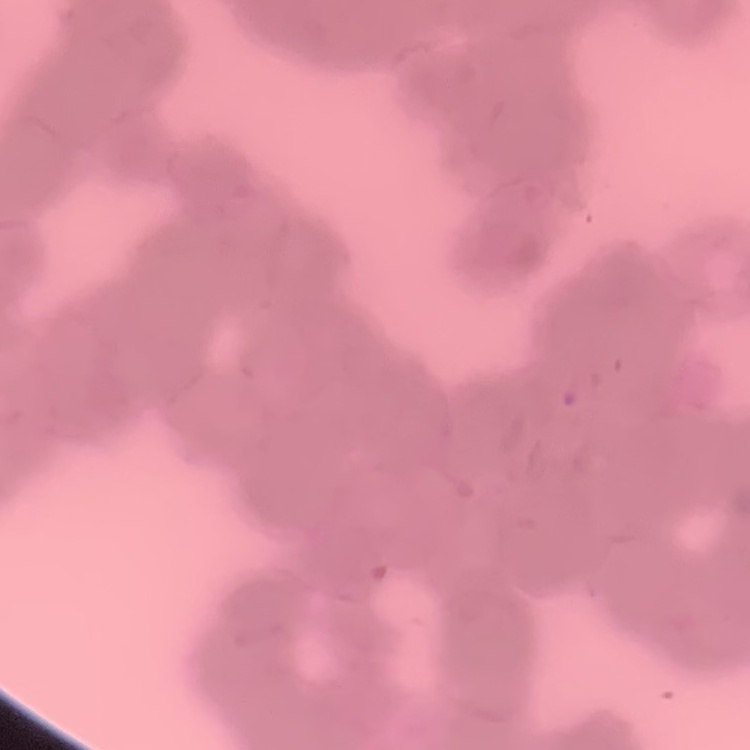

The erythrocytes exhibit rouleaux formation. Stained with either Field's or Giemsa. Thin blood film. Square crop of a larger photomicrograph.